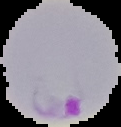

Summary:
  - Image size: 121×127 pixels
  - Result: malaria parasites identified
  - Image type: segmented cell region with the area outside set to black
  - Preparation: thin blood film